Classify this cell by malaria status.
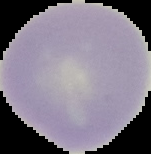
It is uninfected.

image_type: segmented cell region on a black background
image_size: 151×154 pixels
preparation: thin blood film